Comment on the morphology of the red blood cells.
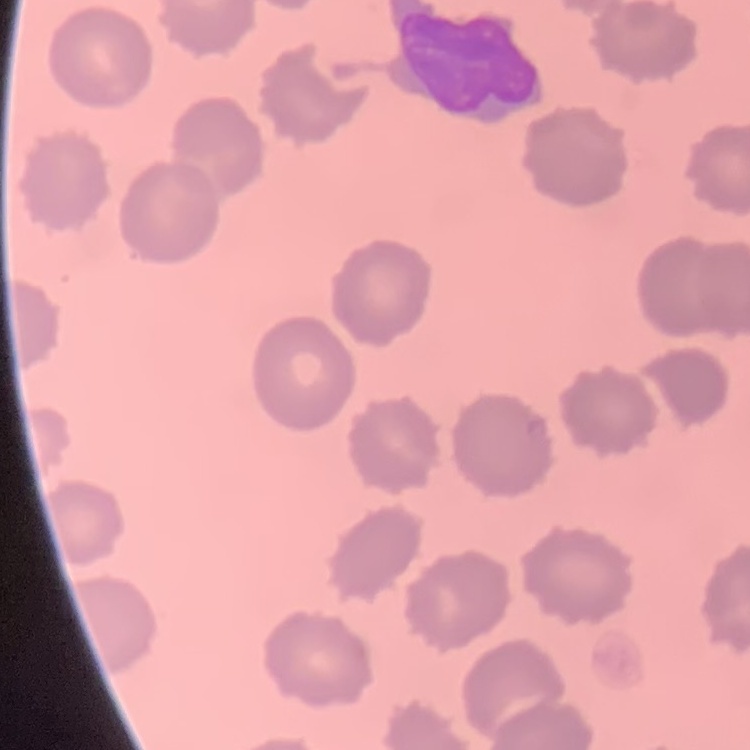
No rouleaux formation.

Summary:
  - Image type: square crop of a larger photomicrograph
  - Stain: Field's or Giemsa
  - Preparation: thin blood smear